Assess this cell for malaria.
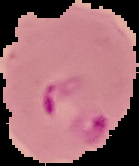
It is parasitized.

Segmented cell region on a black background. Image is 139×166 pixels. From a thin blood film.